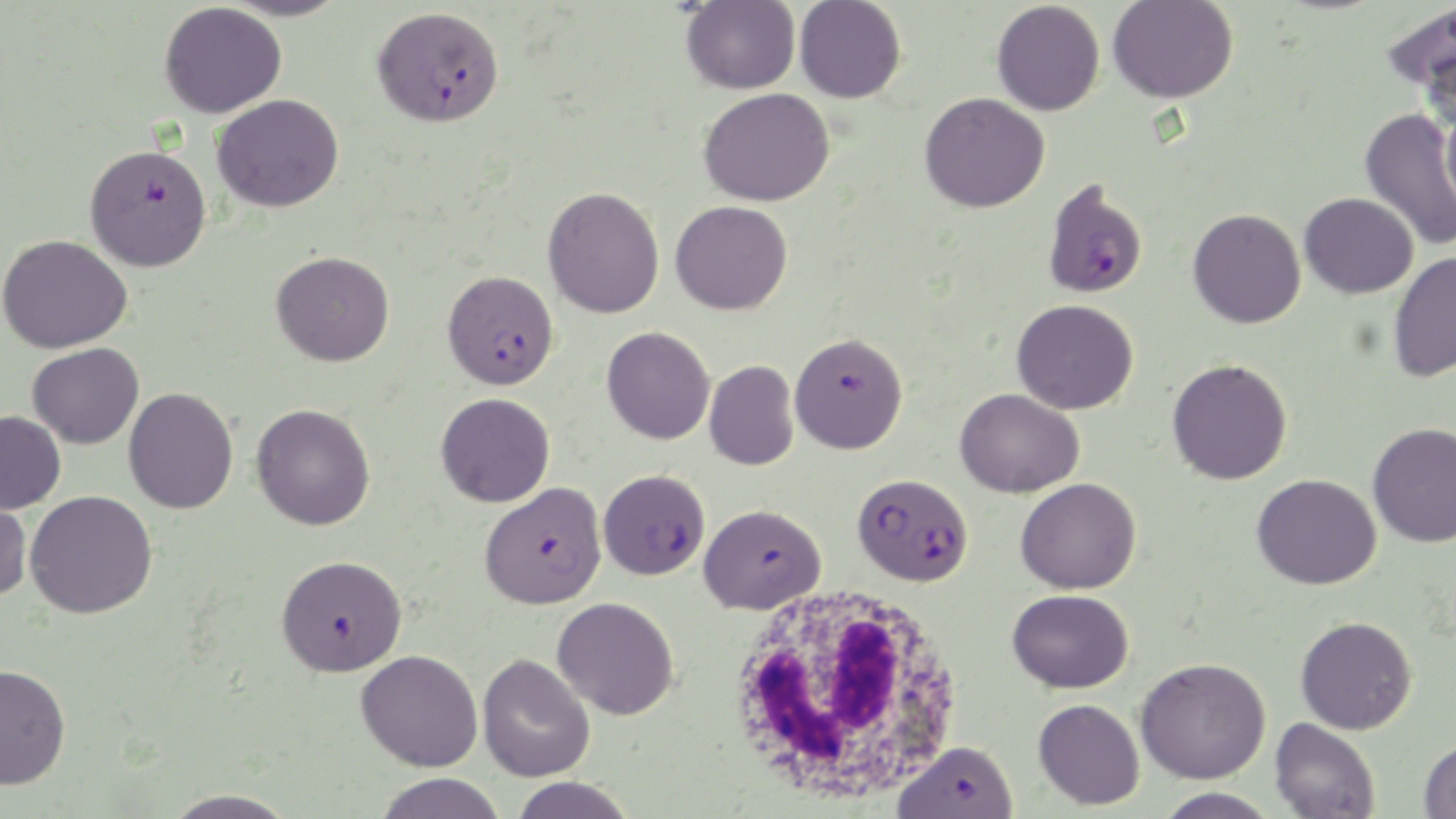

slide-level diagnosis = Plasmodium falciparum
modality = optical microscopy
stain = May-Grünwald-Giemsa
field of view = single
Plasmodium falciparum-infected red blood cell locations = approximate bounding boxes as [x1, y1, x2, y2] in pixels: [373, 6, 504, 128], [86, 142, 212, 271], [1042, 179, 1148, 299], [442, 270, 559, 390], [789, 332, 908, 454], [598, 469, 710, 580], [853, 473, 973, 586], [479, 480, 607, 609], [698, 504, 826, 615], [275, 554, 408, 677], [893, 740, 1019, 817]
preparation = thin blood smear
magnification = 1000x
uninfected red blood cell locations = approximate bounding boxes as [x1, y1, x2, y2] in pixels: [218, 0, 352, 22], [681, 1, 800, 94], [794, 1, 906, 103], [992, 1, 1105, 116], [1107, 1, 1237, 104], [1381, 1, 1456, 112], [159, 2, 287, 119], [699, 87, 835, 207], [920, 91, 1050, 212], [212, 94, 344, 212], [1440, 101, 1456, 222], [1359, 108, 1456, 251], [543, 186, 664, 318], [1299, 192, 1419, 299], [670, 200, 792, 315], [1188, 208, 1306, 328], [1, 234, 132, 353], [271, 251, 394, 367], [1388, 251, 1456, 383], [1012, 299, 1139, 414], [602, 326, 715, 445], [27, 342, 144, 449], [1167, 359, 1292, 485], [705, 360, 799, 470], [124, 387, 239, 514], [955, 388, 1084, 498], [436, 393, 555, 507], [251, 403, 376, 530], [0, 410, 66, 514], [1367, 422, 1456, 547], [1252, 473, 1382, 590], [1016, 477, 1142, 594], [0, 490, 32, 602], [25, 491, 157, 619], [1007, 589, 1133, 693], [552, 596, 679, 720], [1295, 615, 1417, 734], [356, 650, 483, 772], [477, 654, 596, 782], [1136, 657, 1271, 784], [0, 663, 71, 790], [1033, 698, 1145, 810], [1270, 717, 1380, 818], [1419, 737, 1456, 819], [374, 772, 507, 819], [509, 777, 637, 819], [1155, 787, 1281, 819], [161, 788, 299, 819]
white blood cell locations = approximate bounding boxes as [x1, y1, x2, y2] in pixels: [726, 581, 966, 806]
image size = 1456×819 pixels